Locate every Plasmodium vivax-infected red blood cell.
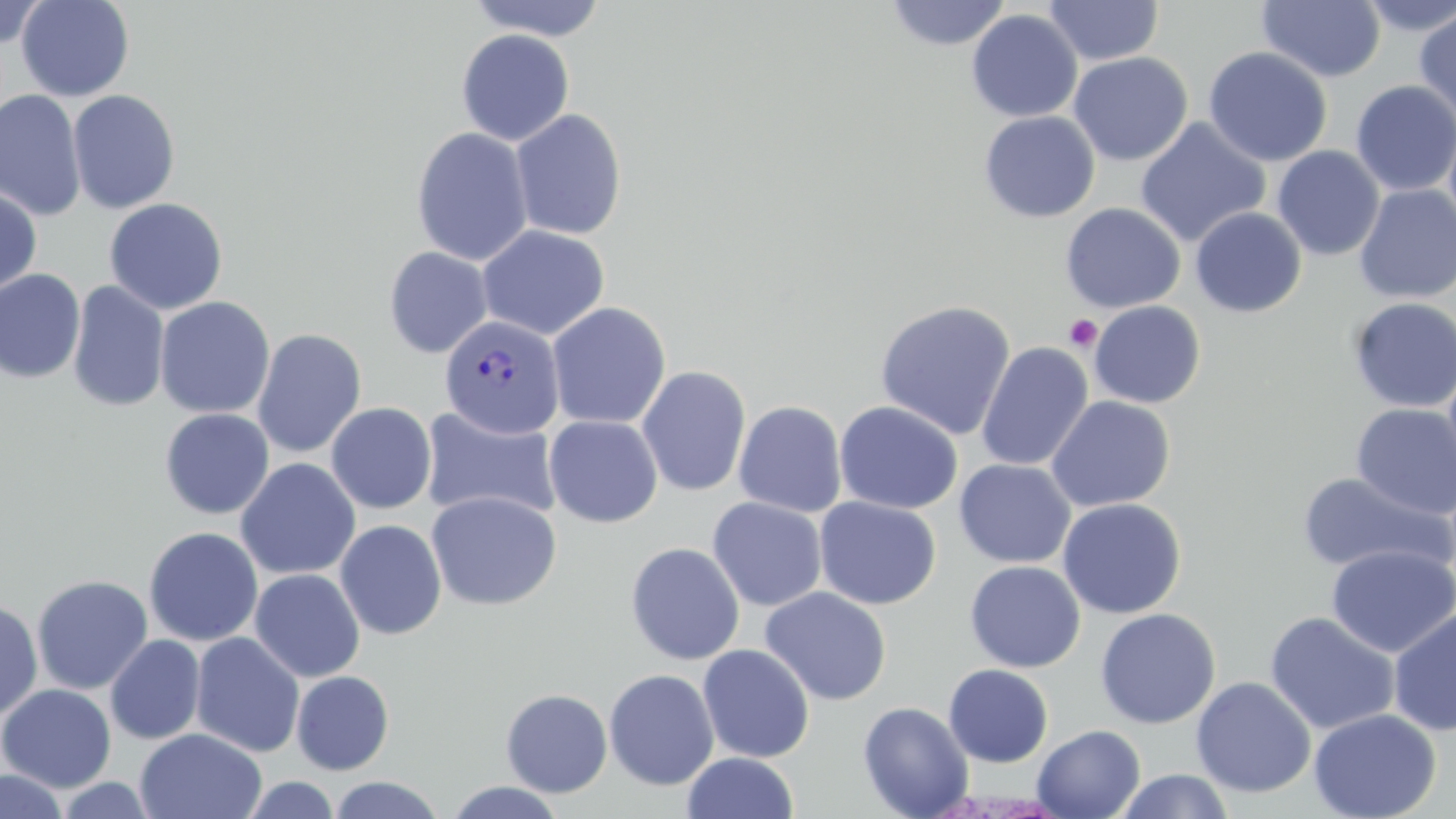
Approximate bounding boxes as [x1, y1, x2, y2] in pixels.
Plasmodium vivax-infected red blood cells: [439, 314, 565, 440].

Summary:
  - Platelet locations: [1064, 314, 1103, 352]
  - Uninfected red blood cell locations: [16, 0, 135, 102], [466, 0, 609, 42], [885, 0, 1011, 50], [1257, 0, 1386, 82], [1355, 0, 1456, 36], [1, 1, 48, 48], [1043, 1, 1165, 66], [1414, 7, 1456, 125], [966, 9, 1083, 122], [456, 28, 575, 146], [1203, 46, 1333, 167], [1068, 52, 1193, 166], [1350, 80, 1456, 196], [0, 89, 86, 221], [67, 89, 181, 214], [510, 108, 628, 241], [978, 111, 1100, 223], [1443, 115, 1456, 238], [1135, 117, 1271, 248], [411, 127, 534, 266], [1271, 145, 1385, 262], [1354, 184, 1456, 304], [0, 187, 42, 298], [104, 197, 228, 315], [1060, 202, 1186, 314], [1190, 207, 1307, 317], [477, 224, 611, 340], [384, 246, 493, 359], [0, 268, 85, 383], [67, 280, 170, 412], [154, 296, 276, 419], [1347, 297, 1456, 413], [874, 300, 1016, 440], [1088, 300, 1206, 408], [546, 302, 671, 429], [252, 328, 367, 458], [975, 341, 1093, 472], [636, 365, 752, 497], [1046, 395, 1175, 512], [733, 400, 847, 518], [834, 400, 964, 515], [326, 402, 437, 514], [1350, 403, 1456, 520], [418, 407, 562, 524], [159, 408, 274, 519], [544, 415, 663, 528], [235, 457, 361, 580], [954, 459, 1076, 568], [1296, 471, 1452, 578], [426, 491, 562, 611], [707, 496, 828, 611], [814, 496, 941, 610], [1057, 497, 1187, 619], [335, 519, 447, 640], [143, 526, 264, 646], [626, 542, 745, 665], [619, 544, 735, 788], [1327, 544, 1456, 658], [964, 560, 1086, 672], [250, 568, 365, 682], [31, 574, 154, 695], [760, 587, 892, 706], [0, 598, 43, 722], [1095, 607, 1221, 729], [1388, 608, 1456, 736], [1264, 611, 1400, 735], [190, 632, 305, 758], [105, 635, 206, 744], [697, 644, 815, 762], [943, 664, 1054, 767], [604, 669, 720, 791], [291, 671, 394, 775], [1191, 677, 1316, 798], [1, 683, 116, 792], [500, 688, 613, 797], [858, 701, 975, 819], [1308, 708, 1442, 819], [1032, 724, 1145, 819], [135, 727, 267, 819], [682, 752, 800, 819], [0, 769, 69, 819], [1114, 769, 1235, 819], [240, 776, 342, 818], [328, 776, 446, 818], [55, 777, 157, 818], [443, 781, 568, 818]
  - Slide-level diagnosis: Plasmodium vivax
  - Magnification: 1000x
  - Stain: May-Grünwald-Giemsa
  - Modality: optical microscopy
  - Image size: 1456×819 pixels
  - Preparation: thin blood film
  - Field of view: single